State the preparation type.
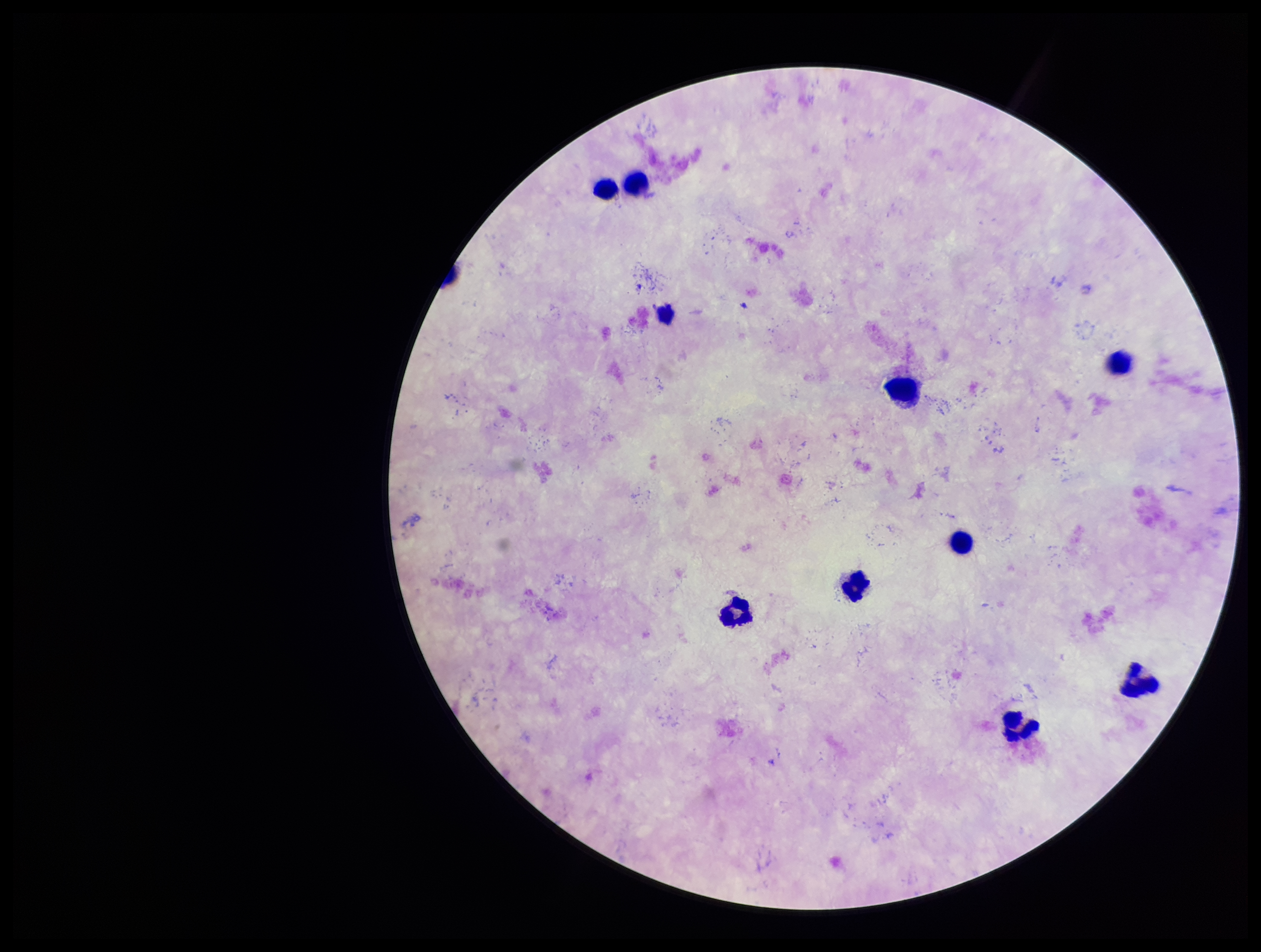
It is a thick blood smear.

Summary:
  - Patient malaria status: negative
  - Stain: Giemsa
  - Capture: smartphone photograph through the microscope eyepiece
  - Field of view: one from this slide
  - Parasite count: 0
  - Image size: 1261×952 pixels
  - Plasmodium parasites: none identified
  - Leukocyte count: 10